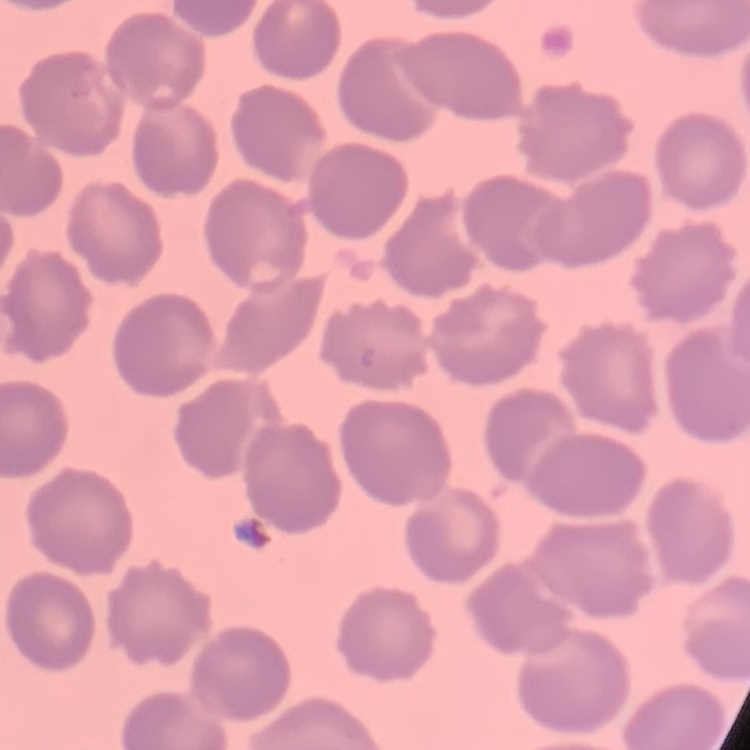
red blood cell morphology = no rouleaux formation
image type = one tile cut from a larger photomicrograph
preparation = thin blood film
stain = Field's or Giemsa